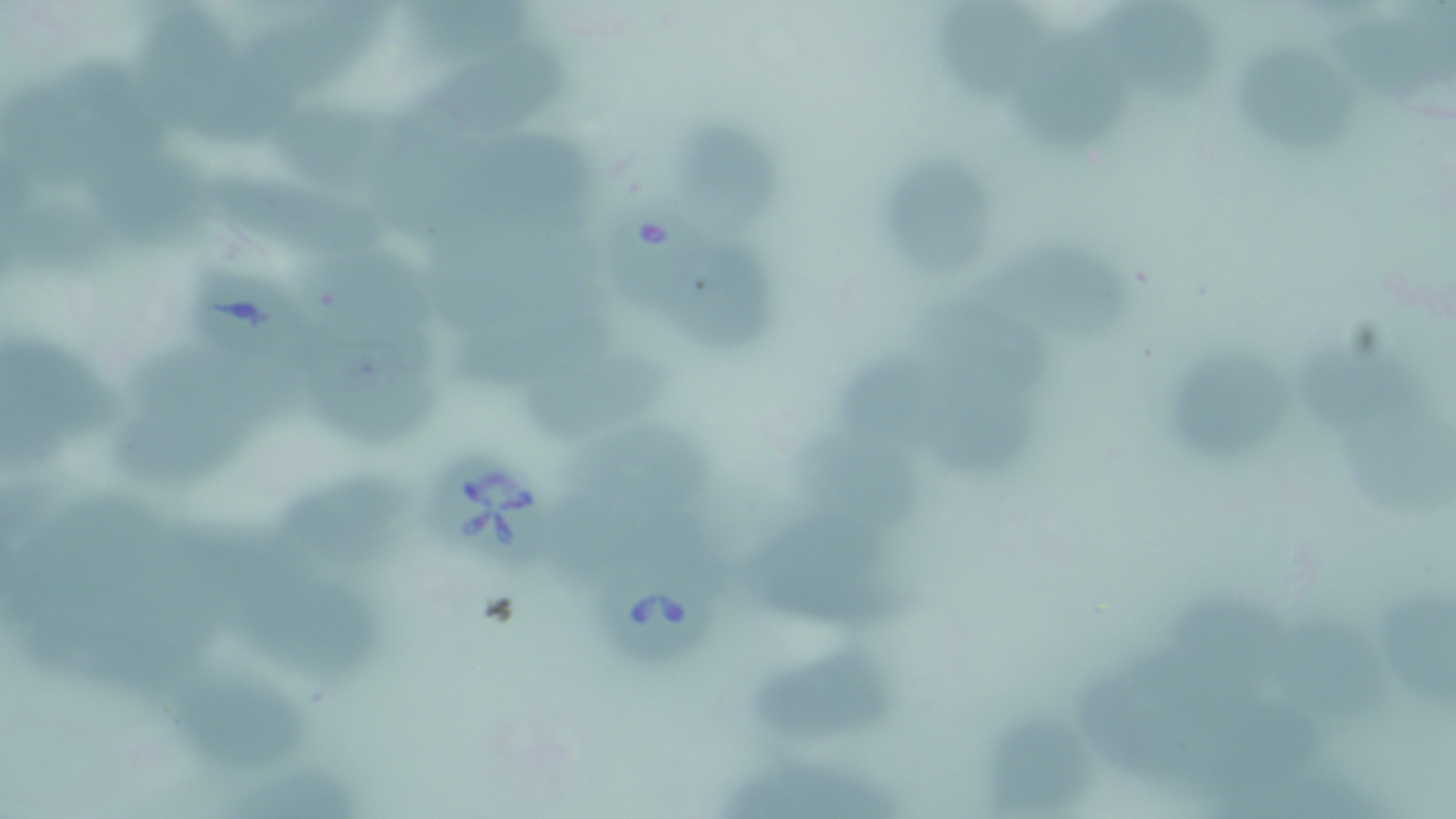

Summary:
  - Coordinate format: approximate bounding boxes as [x1, y1, x2, y2] in pixels
  - Babesia divergens-infected red blood cell locations: [605, 196, 715, 312], [185, 265, 300, 363], [441, 460, 551, 580], [595, 554, 719, 667]
  - Uninfected red blood cell locations: [405, 0, 555, 70], [937, 0, 1058, 109], [1109, 0, 1224, 108], [137, 3, 263, 143], [244, 3, 391, 109], [1345, 18, 1444, 107], [1016, 19, 1142, 151], [1241, 42, 1357, 157], [430, 47, 582, 149], [47, 57, 180, 159], [267, 100, 430, 198], [684, 127, 787, 237], [458, 129, 599, 235], [68, 132, 214, 246], [885, 159, 1005, 282], [189, 168, 393, 269], [433, 214, 602, 324], [314, 241, 437, 352], [983, 246, 1144, 337], [680, 247, 779, 351], [914, 290, 1070, 396], [460, 299, 623, 399], [0, 333, 134, 470], [310, 336, 449, 444], [138, 337, 319, 435], [1303, 342, 1436, 442], [523, 348, 677, 440], [837, 349, 964, 452], [1173, 354, 1296, 462], [929, 377, 1050, 485], [117, 392, 269, 491], [1349, 412, 1453, 517], [566, 421, 728, 519], [798, 431, 932, 532], [275, 462, 418, 584], [543, 479, 724, 580], [745, 510, 914, 633], [147, 517, 283, 632], [243, 570, 382, 680], [1178, 590, 1308, 688], [1386, 592, 1456, 718], [1274, 615, 1402, 731], [1127, 628, 1283, 741], [755, 640, 901, 747], [154, 663, 319, 769], [1072, 676, 1195, 782], [1188, 694, 1349, 804], [985, 717, 1094, 818], [229, 747, 367, 819], [731, 755, 908, 819]
  - Slide-level diagnosis: Babesia divergens
  - Modality: light microscopy
  - Stain: May-Grünwald-Giemsa
  - Field of view: single
  - Preparation: thin blood film
  - Magnification: 1000x
  - Image size: 1456×819 pixels